Locate every Plasmodium ovale-infected red blood cell.
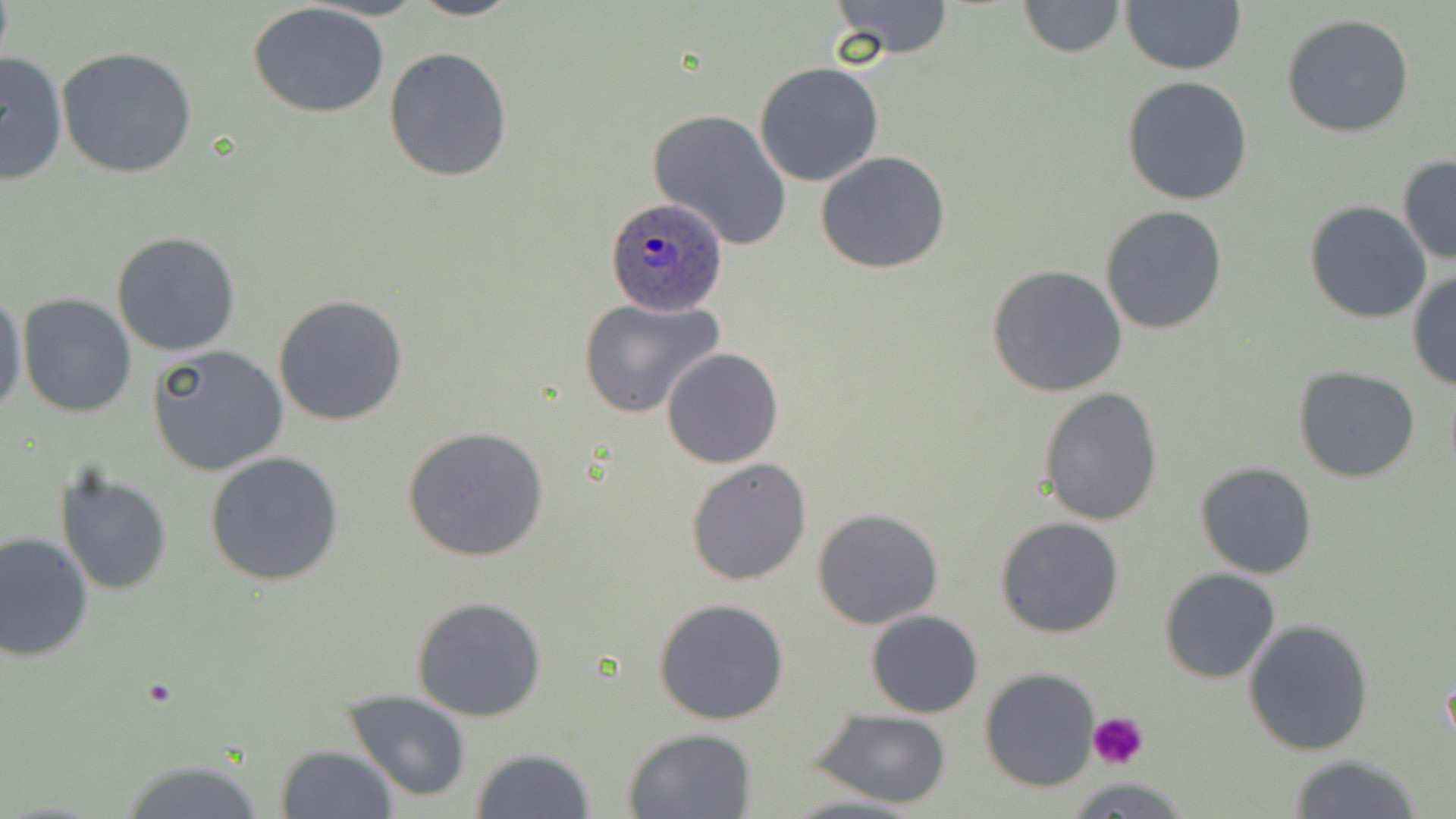
Approximate bounding boxes as (x1,y1)-(x2,y2) corner pairs in pixels.
Plasmodium ovale-infected red blood cells: (601,196)-(731,315).

Platelet locations: (1086,712)-(1148,769). Uninfected red blood cell locations: (407,0)-(521,22), (829,0)-(956,58), (1016,0)-(1126,57), (1121,0)-(1246,74), (247,3)-(391,117), (1281,15)-(1415,138), (57,46)-(200,179), (384,46)-(514,182), (0,50)-(70,183), (754,62)-(883,186), (1121,77)-(1253,206), (648,108)-(793,251), (815,152)-(952,275), (1397,156)-(1455,266), (1304,202)-(1432,323), (1100,205)-(1227,334), (110,232)-(241,357), (986,265)-(1128,398), (1408,269)-(1456,389), (0,288)-(26,419), (18,294)-(136,418), (274,295)-(408,426), (578,296)-(725,418), (147,344)-(287,476), (661,346)-(784,468), (1294,367)-(1422,481), (1038,387)-(1163,525), (401,424)-(553,562), (204,451)-(345,586), (686,458)-(812,585), (1195,461)-(1317,578), (56,471)-(173,593), (811,508)-(944,629), (994,517)-(1123,638), (0,530)-(94,662), (1159,569)-(1280,683), (411,596)-(549,721), (653,597)-(789,724), (865,610)-(983,718), (1243,618)-(1373,757), (980,668)-(1103,791), (343,690)-(473,803), (812,710)-(953,807), (622,727)-(757,817), (276,743)-(397,818), (469,748)-(598,819), (1287,755)-(1426,818), (114,758)-(273,817), (777,792)-(929,819). Slide-level diagnosis: Plasmodium ovale. Thin blood smear. May-Grünwald-Giemsa stain. Captured at 1000x magnification. Image is 1456×819 pixels. Single field of view. Optical microscopy.